Assess the morphology of the red blood cells.
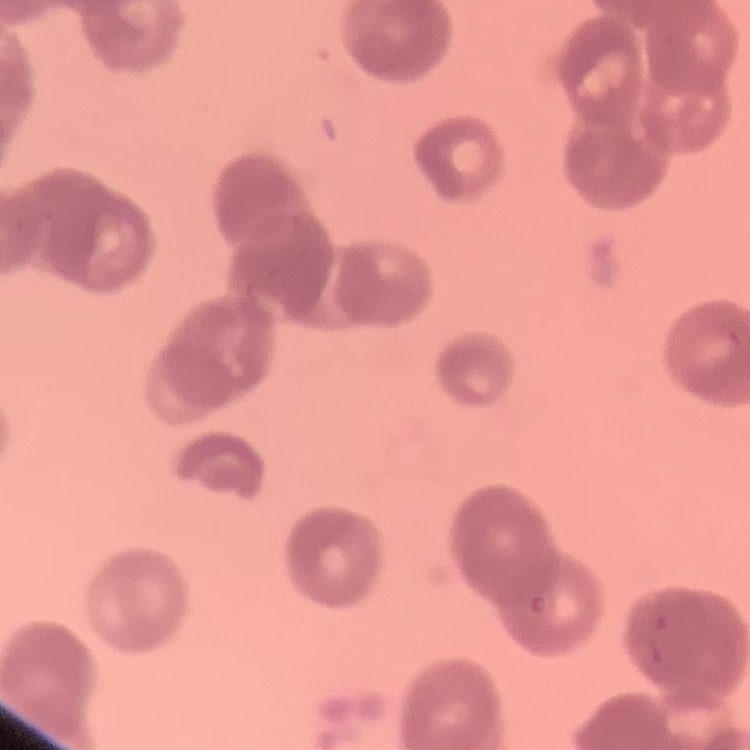
They show rouleaux formation.

Summary:
  - Preparation: thin blood smear
  - Stain: Field's or Giemsa
  - Image type: one tile cut from a larger photomicrograph